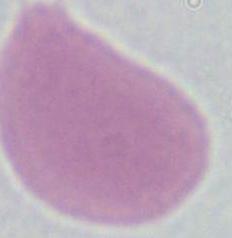

modality = micrograph
magnification = 1000x
identification = erythrocyte